Name the parasite shown.
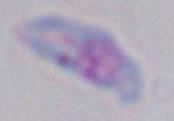

This is Toxoplasma gondii.

Summary:
  - Modality: micrograph
  - Magnification: 1000x